Assess for Plasmodium parasites.
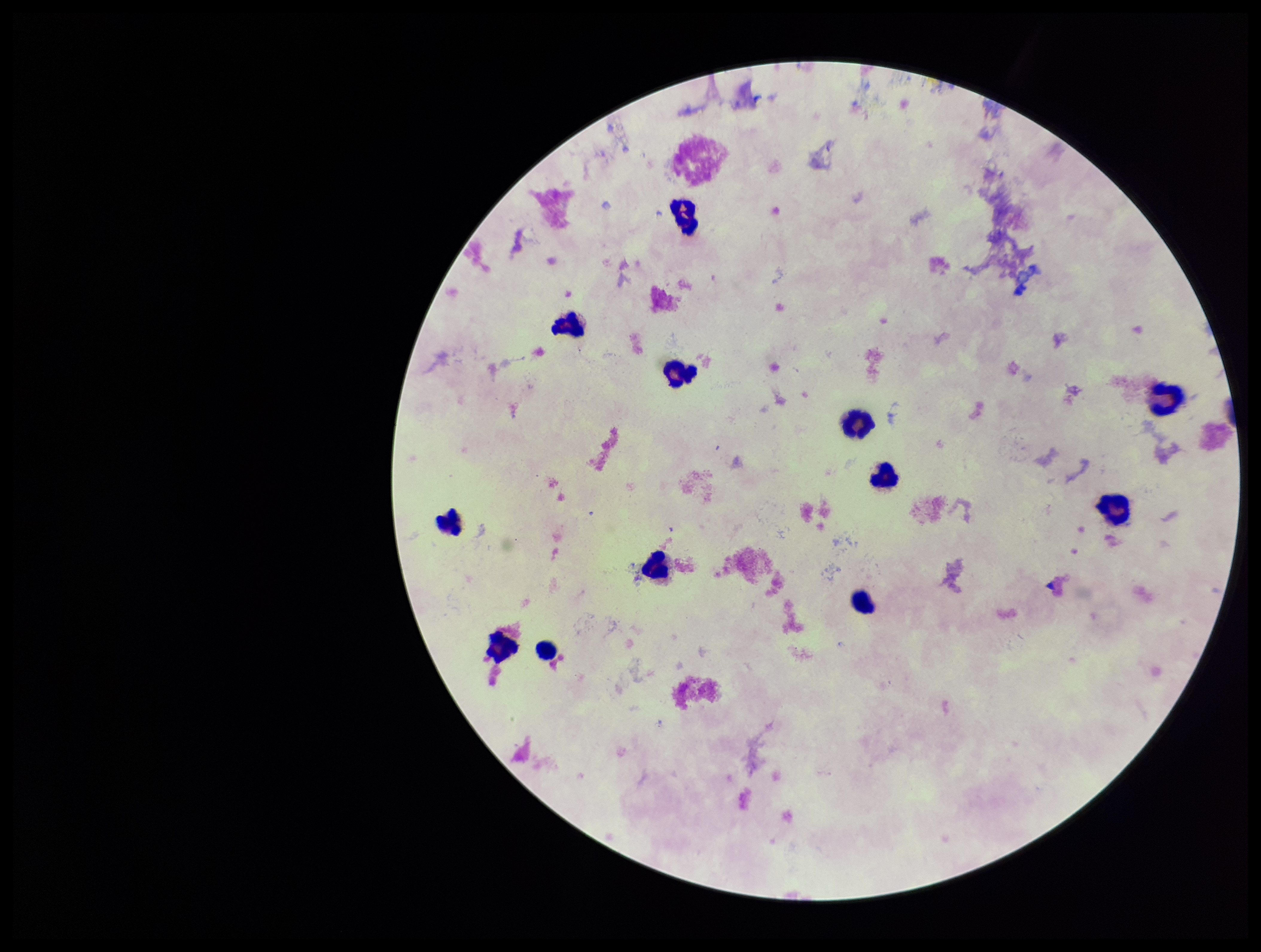
None detected.

Summary:
  - Leukocyte count: 12
  - Field of view: single
  - Preparation: thick smear
  - Patient malaria status: negative
  - Parasite count: 0
  - Image size: 1261×952 pixels
  - Stain: Giemsa
  - Capture: smartphone photograph through the microscope eyepiece